Describe the morphology of the red blood cells.
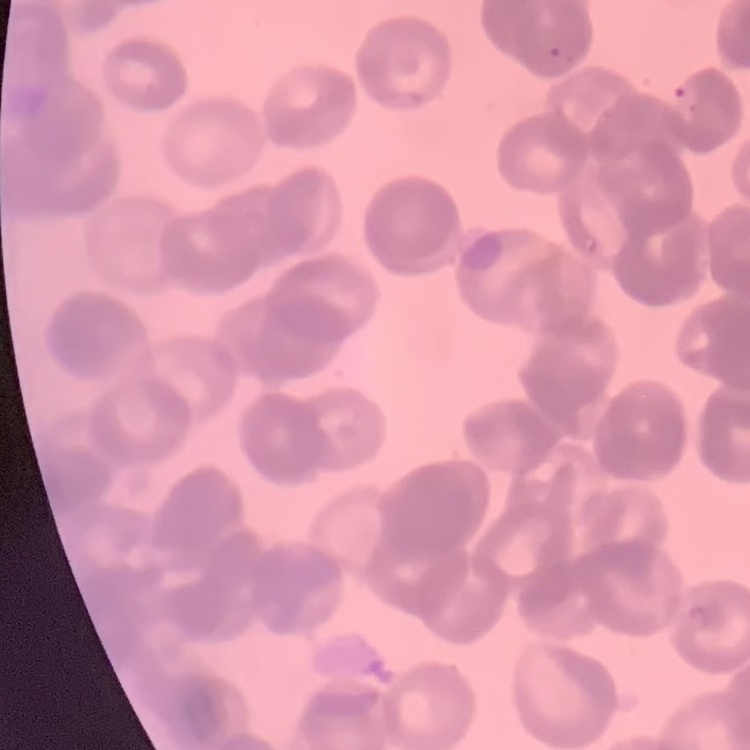
They show rouleaux formation.

One tile cut from a larger photomicrograph. Thin blood film. Stained with either Field's or Giemsa.